Assess this cell for malaria.
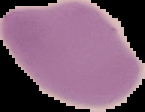
Uninfected.

Summary:
  - Preparation: thin blood film
  - Image type: cell region segmented out of the field of view; surrounding area masked to black
  - Image size: 145×112 pixels